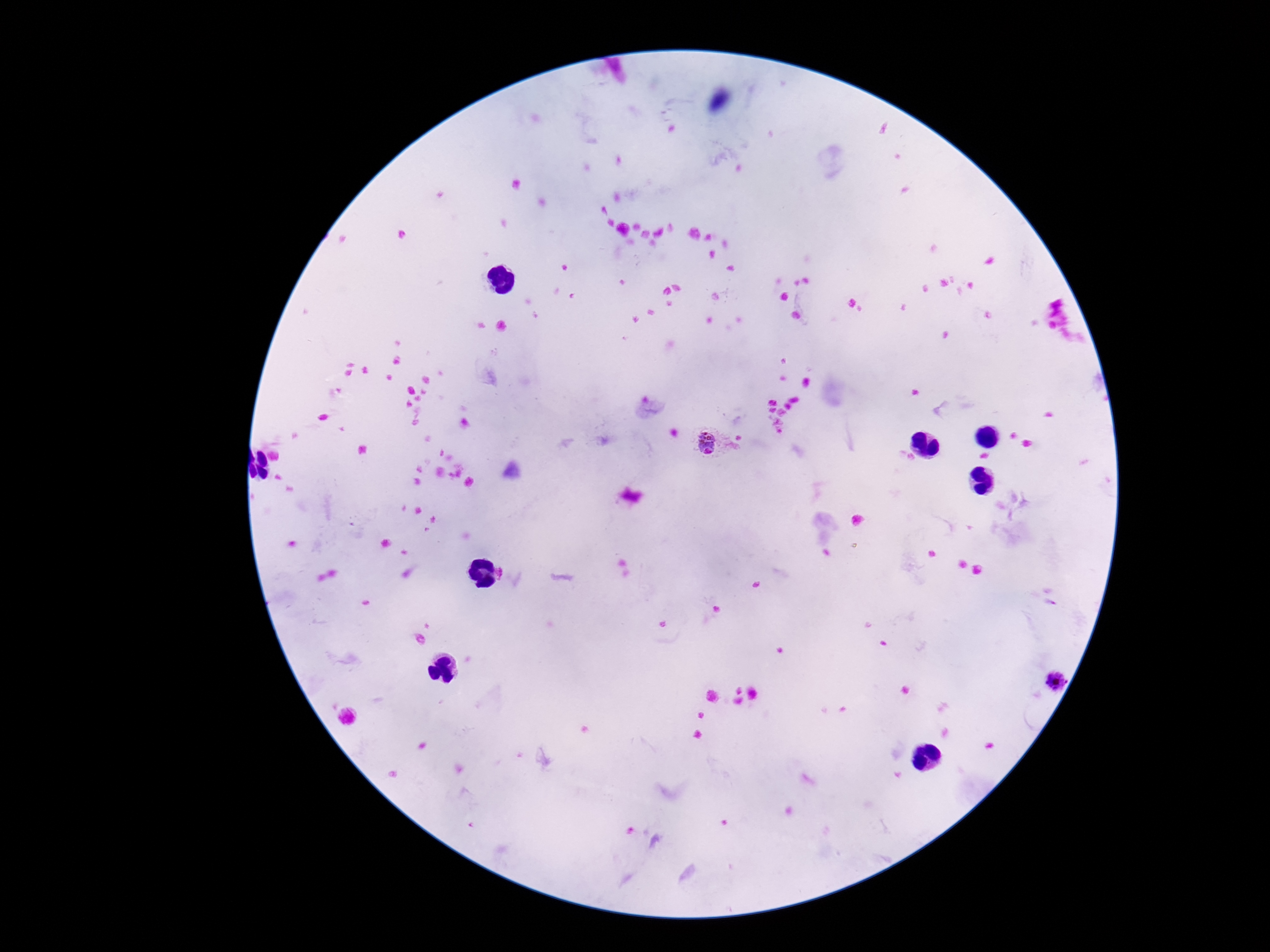

Approximate object centers, in pixels from the top-left corner.
Summary:
  - Plasmodium parasite locations: (x=710, y=444), (x=1058, y=681)
  - Image size: 1270×952 pixels
  - Patient malaria status: positive
  - Field of view: single
  - Stain: Giemsa
  - Magnification: 100x
  - Preparation: thick blood smear
  - Capture: smartphone camera through the microscope eyepiece